Mark where platelets are.
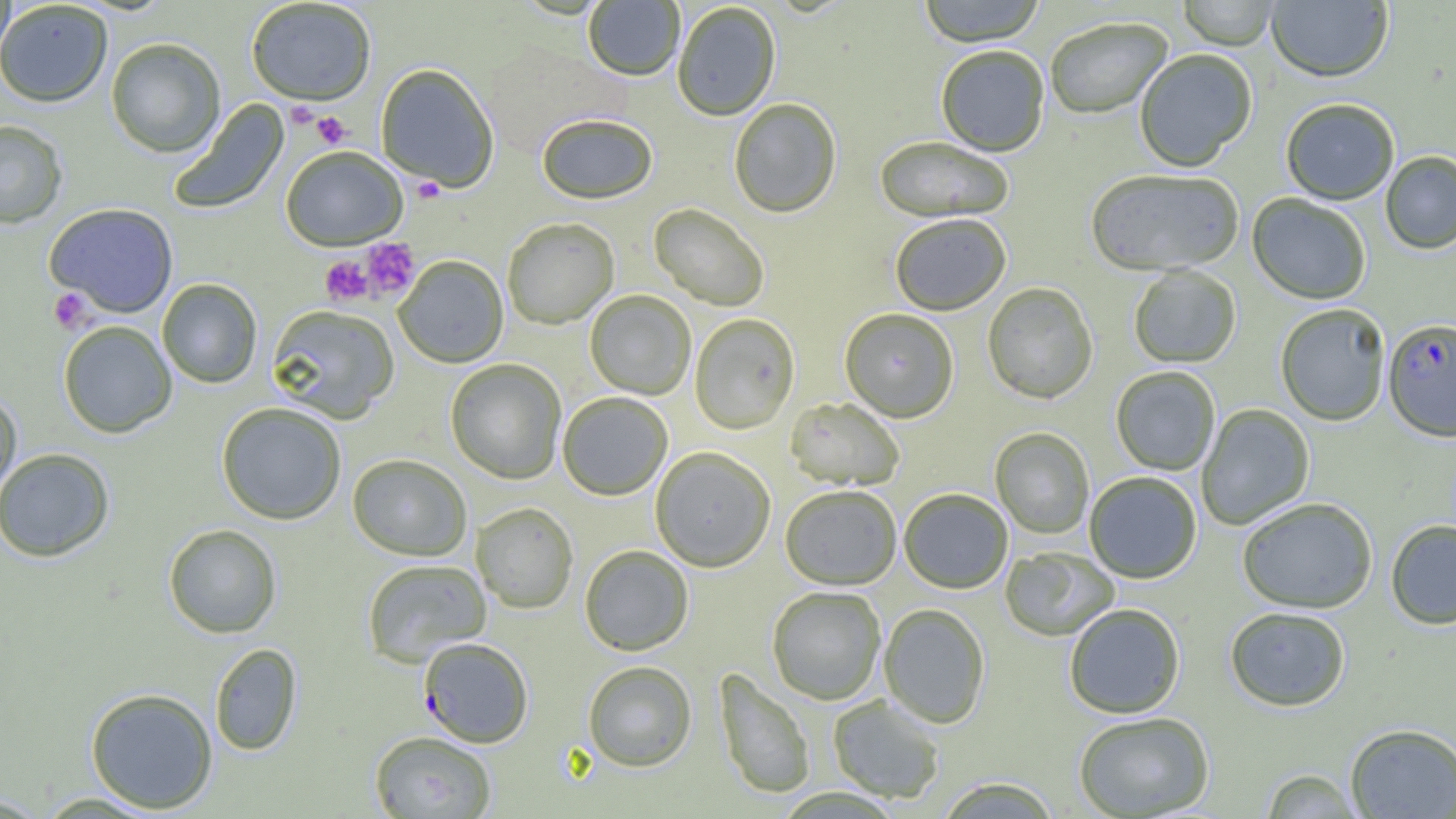

Approximate bounding boxes as (x1,y1)-(x2,y2) corner pairs in pixels.
Platelets: (286,101)-(320,130), (311,111)-(351,149), (411,177)-(446,203), (360,238)-(419,298), (320,256)-(373,306), (48,288)-(96,333).

Plasmodium falciparum-infected red blood cell locations: (1382,321)-(1456,444), (418,638)-(533,748). Uninfected red blood cell locations: (0,0)-(15,69), (246,0)-(376,106), (917,0)-(1046,49), (1177,0)-(1280,52), (1266,0)-(1393,85), (0,1)-(113,108), (583,1)-(684,83), (673,3)-(781,123), (1045,19)-(1174,121), (106,38)-(225,158), (936,48)-(1050,158), (1135,51)-(1257,173), (376,65)-(499,193), (167,99)-(290,216), (729,100)-(841,219), (1281,101)-(1399,206), (537,115)-(658,206), (0,119)-(68,229), (875,138)-(1014,226), (280,148)-(407,251), (1381,152)-(1456,255), (1086,171)-(1243,278), (1247,194)-(1370,306), (44,203)-(178,318), (649,204)-(769,311), (890,216)-(1010,316), (502,219)-(619,330), (393,256)-(509,369), (1129,266)-(1241,369), (157,279)-(262,388), (982,283)-(1098,405), (585,291)-(696,400), (266,305)-(399,423), (1276,305)-(1390,427), (840,310)-(959,425), (689,315)-(800,435), (58,321)-(177,438), (445,360)-(566,485), (1110,367)-(1220,476), (0,391)-(22,505), (558,393)-(672,501), (785,398)-(904,492), (216,403)-(346,525), (1197,404)-(1315,530), (990,428)-(1094,539), (0,448)-(115,562), (650,448)-(775,573), (347,454)-(471,561), (1084,473)-(1202,584), (781,487)-(901,592), (899,490)-(1012,595), (1238,500)-(1377,615), (471,503)-(578,614), (1386,521)-(1456,631), (163,523)-(282,638), (579,546)-(694,656), (1000,548)-(1119,642), (362,559)-(491,666), (767,587)-(886,705), (879,604)-(990,729), (1064,604)-(1185,719), (1225,608)-(1351,713), (210,643)-(303,756), (583,661)-(697,773), (713,668)-(815,801), (85,687)-(218,814), (828,695)-(945,804), (1074,713)-(1214,819), (1345,724)-(1456,818), (369,731)-(496,819), (1260,769)-(1363,818), (935,777)-(1063,818), (32,792)-(164,817), (0,794)-(52,818). Slide-level diagnosis: Plasmodium falciparum. Image is 1456×819 pixels. Single field of view. Captured at 1000x magnification. Thin blood film. Light microscopy.